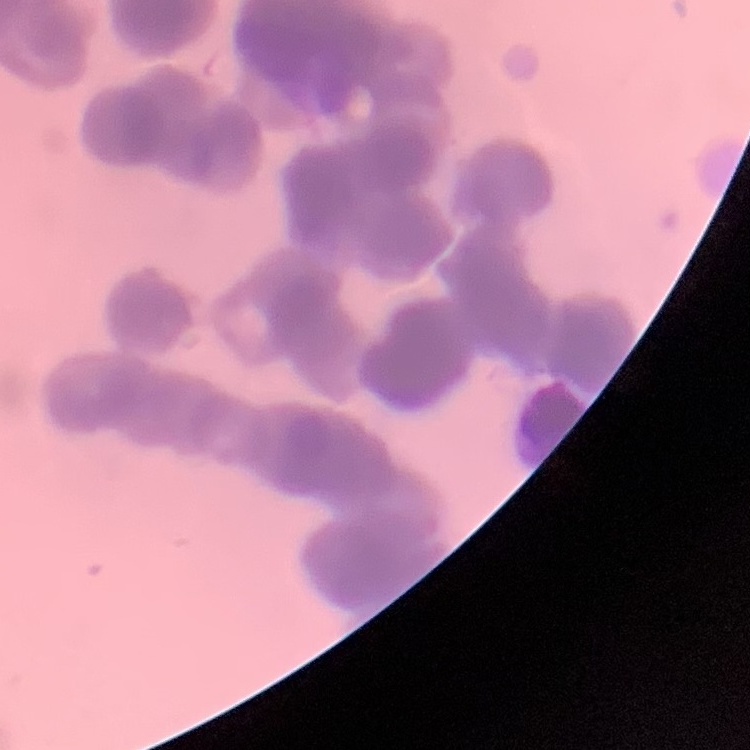

erythrocyte morphology = rouleaux formation
stain = Field's or Giemsa
preparation = thin blood film
image type = one tile cut from a larger photomicrograph